State the blood parasite species.
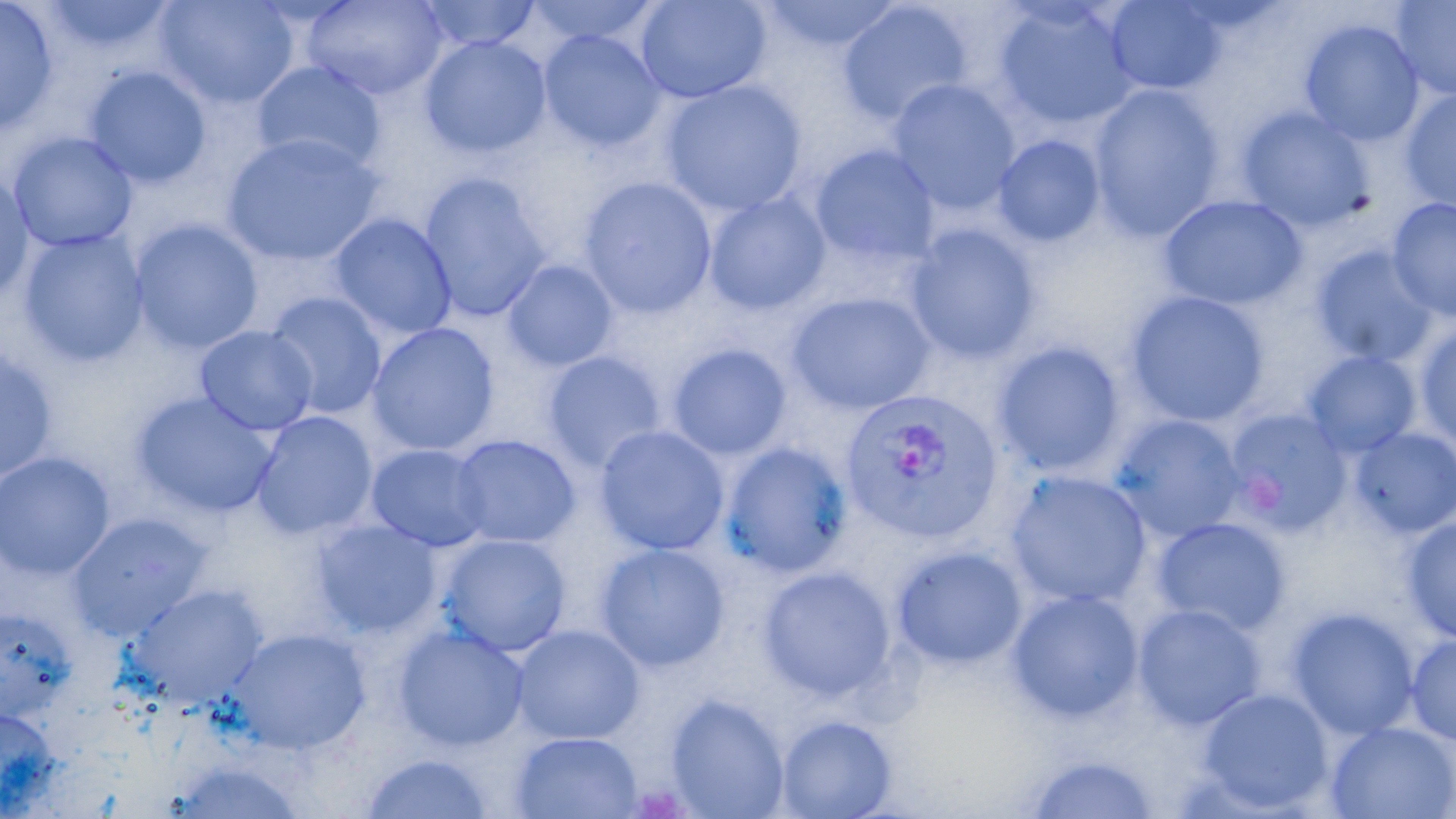

Plasmodium vivax.

Approximate bounding boxes as [x1, y1, x2, y2] in pixels. Platelet locations: [628, 785, 693, 818]. Uninfected red blood cell locations: [417, 0, 541, 52], [525, 0, 661, 48], [636, 0, 770, 103], [757, 0, 906, 53], [1104, 0, 1226, 95], [1391, 0, 1456, 101], [0, 1, 58, 134], [39, 1, 179, 54], [155, 1, 299, 109], [302, 1, 447, 100], [837, 1, 975, 127], [993, 1, 1138, 131], [1300, 18, 1424, 147], [538, 29, 666, 152], [420, 35, 551, 158], [251, 59, 387, 175], [85, 66, 211, 189], [888, 79, 1021, 216], [660, 80, 807, 217], [1089, 85, 1224, 242], [1401, 89, 1456, 212], [1237, 107, 1374, 232], [9, 132, 138, 252], [223, 132, 384, 267], [993, 135, 1105, 248], [809, 145, 940, 269], [0, 169, 33, 303], [419, 173, 551, 321], [580, 176, 717, 319], [704, 193, 830, 316], [1158, 195, 1307, 311], [1388, 198, 1456, 322], [329, 214, 457, 340], [130, 219, 264, 355], [903, 223, 1042, 364], [19, 229, 149, 367], [1312, 245, 1439, 367], [502, 260, 618, 371], [786, 291, 936, 414], [1125, 291, 1270, 427], [264, 292, 387, 419], [367, 323, 499, 456], [1414, 323, 1456, 451], [195, 325, 318, 436], [993, 341, 1126, 475], [667, 343, 792, 461], [0, 347, 58, 482], [1303, 350, 1420, 458], [542, 351, 667, 473], [132, 392, 280, 519], [1224, 408, 1352, 535], [250, 411, 378, 540], [1111, 415, 1246, 540], [595, 426, 729, 556], [1350, 427, 1456, 538], [451, 435, 580, 548], [720, 442, 852, 578], [368, 444, 491, 551], [0, 452, 115, 579], [1005, 471, 1151, 608], [68, 514, 210, 641], [1152, 517, 1290, 637], [1401, 517, 1456, 643], [312, 519, 441, 638], [439, 533, 571, 656], [595, 543, 730, 672], [891, 545, 1027, 669], [758, 566, 896, 701], [128, 584, 268, 707], [1006, 589, 1143, 723], [1133, 603, 1266, 730], [0, 607, 77, 720], [1287, 607, 1420, 739], [511, 624, 645, 744], [393, 626, 529, 752], [228, 627, 371, 755], [1405, 635, 1456, 745], [1195, 687, 1334, 815], [665, 695, 789, 818], [0, 707, 63, 813], [775, 714, 898, 819], [1325, 721, 1456, 819], [509, 730, 644, 818], [1020, 752, 1163, 818], [359, 753, 497, 818], [166, 758, 309, 819]. Plasmodium vivax-infected red blood cell locations: [840, 390, 1001, 542]. Image is 1456×819 pixels. Thin blood film. May-Grünwald-Giemsa stain. One field of a larger specimen. Optical microscopy. 1000x magnification.